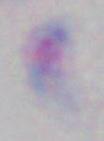

Summary:
  - Modality: micrograph
  - Identification: Toxoplasma gondii
  - Magnification: 1000x